Point out each Plasmodium parasite.
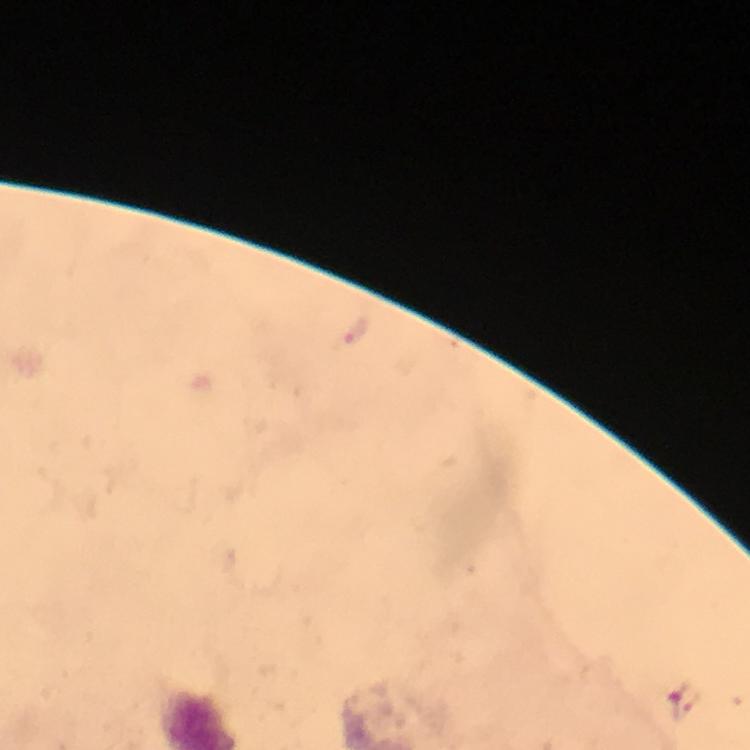

Approximate centers as {x, y} in pixels.
Plasmodium parasites: {355, 328}, {684, 701}.

Cropped region of a single field of view. Thick smear. From a diagnostic examination for malaria. At 100x magnification. Smartphone photograph taken through a microscope. Immersion oil applied. Image is 750×750 pixels. Giemsa stain.